Locate every blood parasite and identify its species.
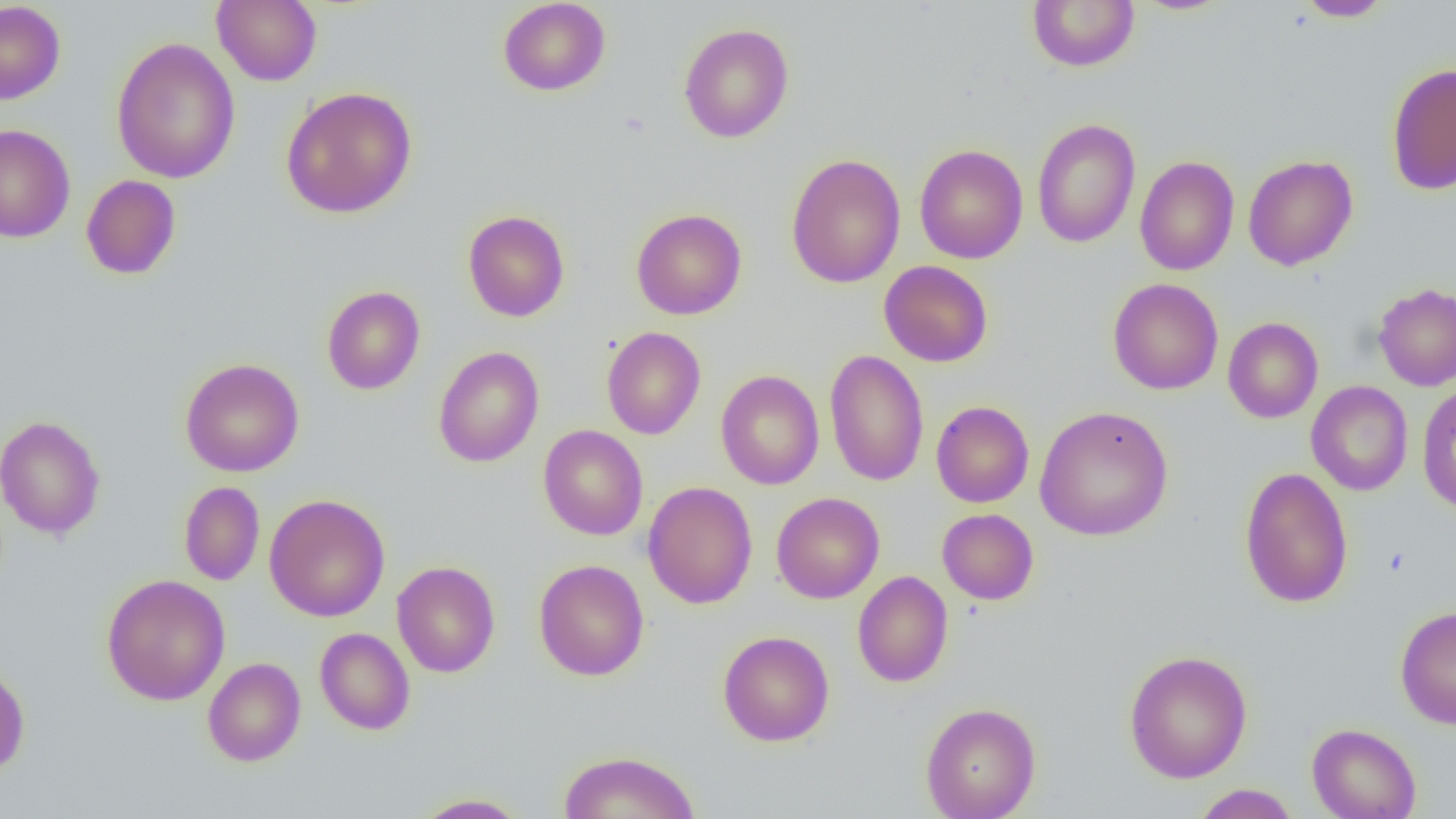

No blood parasites seen.

Approximate bounding boxes as (x1,y1)-(x2,y2) corner pairs in pixels. Uninfected red blood cell locations: (212,0)-(322,86), (497,0)-(611,96), (1027,0)-(1139,72), (1130,0)-(1237,16), (1294,0)-(1394,21), (0,1)-(66,104), (678,22)-(794,143), (111,36)-(241,184), (1386,62)-(1456,195), (280,86)-(418,219), (1032,118)-(1140,248), (0,123)-(75,243), (914,144)-(1028,264), (785,153)-(906,288), (1243,155)-(1358,271), (1134,156)-(1239,276), (81,175)-(181,280), (631,208)-(747,320), (462,210)-(570,322), (879,260)-(993,367), (1108,278)-(1224,395), (1373,283)-(1456,391), (321,286)-(426,395), (1223,317)-(1323,423), (602,326)-(706,440), (433,346)-(545,468), (825,349)-(929,487), (179,358)-(305,477), (715,370)-(825,489), (1306,380)-(1413,496), (1416,382)-(1456,514), (931,401)-(1034,507), (1034,405)-(1174,542), (0,414)-(106,540), (538,425)-(648,540), (1239,466)-(1354,609), (643,481)-(757,609), (178,482)-(265,585), (771,492)-(885,603), (264,493)-(390,622), (937,508)-(1039,605), (534,559)-(649,681), (391,561)-(501,678), (853,571)-(953,687), (101,574)-(230,706), (1395,605)-(1456,728), (314,628)-(415,735), (717,630)-(835,747), (1123,649)-(1253,784), (203,657)-(306,766), (0,661)-(30,776), (921,701)-(1040,819), (1306,723)-(1421,819), (559,750)-(701,819), (1191,784)-(1300,819), (412,793)-(532,818). Slide-level diagnosis: negative for blood parasites. Image is 1456×819 pixels. Optical microscopy. Thin blood film. Single field of view. Captured at 1000x magnification.